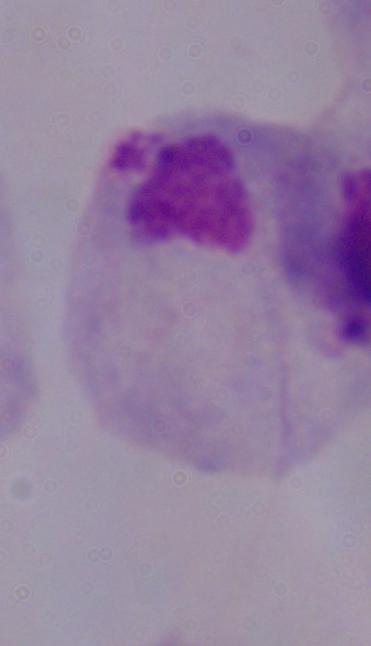
{
  "identification": "trichomonad",
  "modality": "micrograph",
  "magnification": "1000x"
}